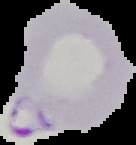
From a thin blood film. Image is 136×145 pixels. The area outside the segmented cell region is set to black. Malaria status: parasitized.